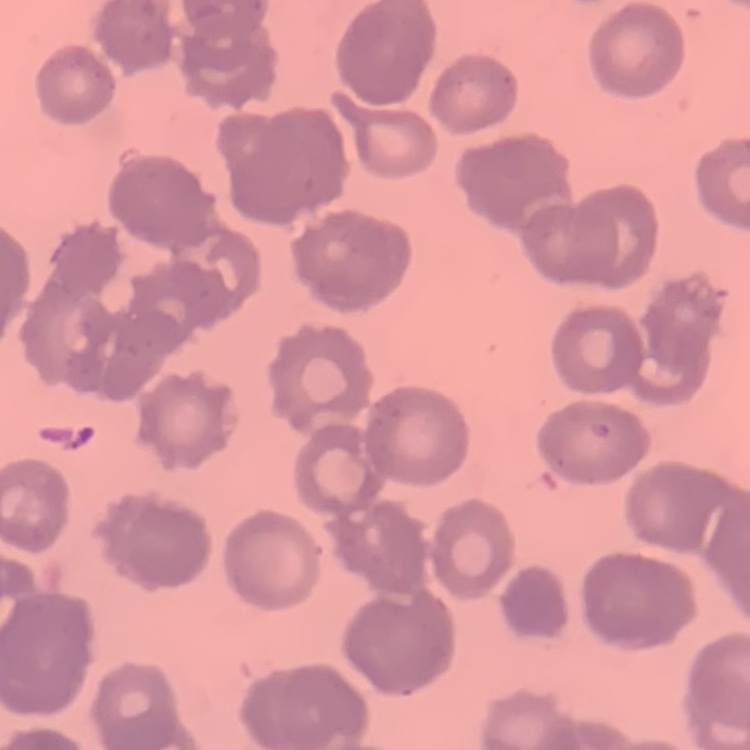

{
  "red_blood_cell_morphology": "rouleaux formation",
  "stain": "Field's or Giemsa",
  "preparation": "thin blood smear",
  "image_type": "one tile cut from a larger photomicrograph"
}